State the blood parasite species.
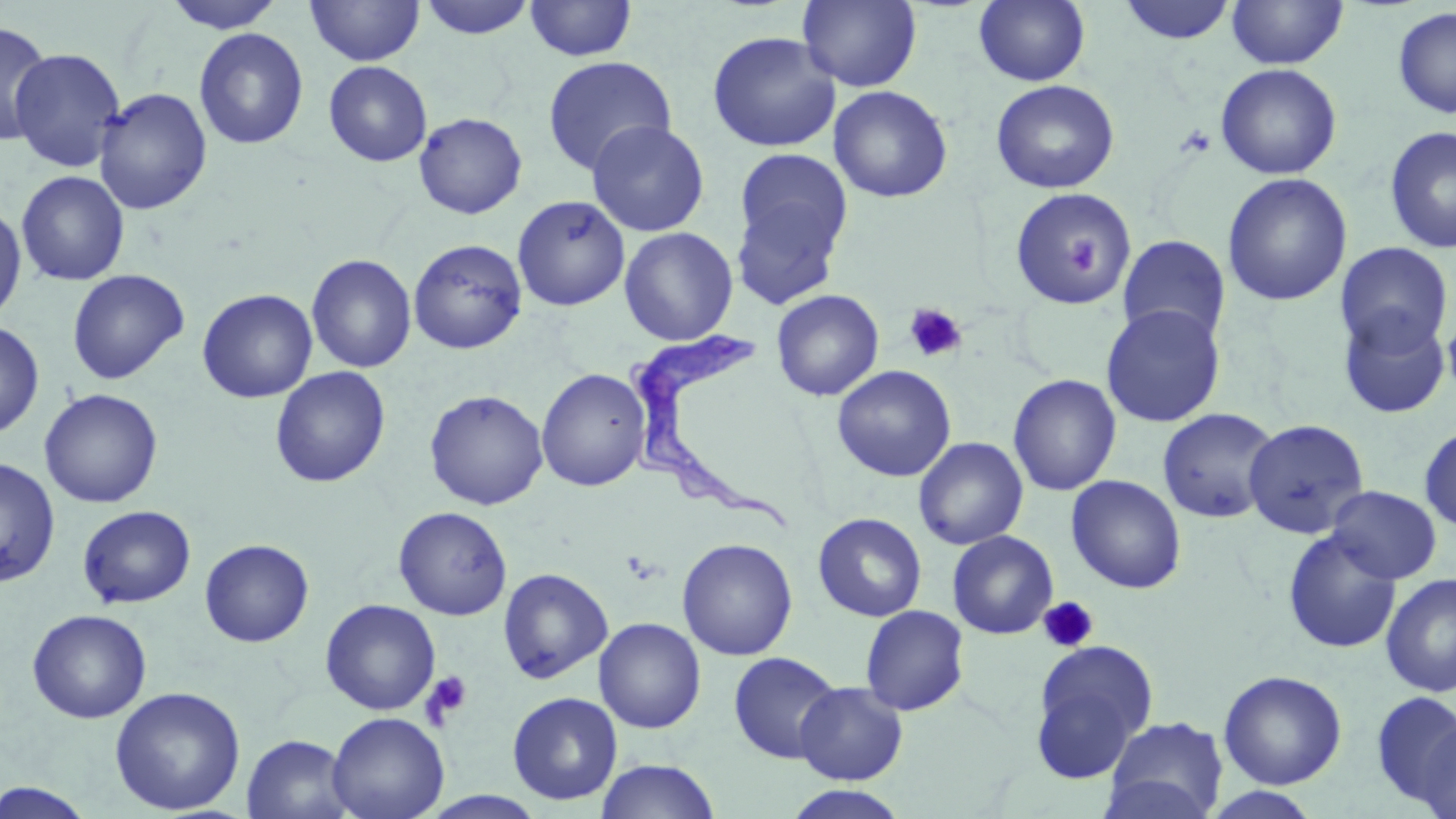
Trypanosoma brucei.

Approximate bounding boxes as (x1, y1, x2, y2) in pixels. Trypanosoma brucei locations: (625, 316, 796, 535). Uninfected red blood cell locations: (162, 0, 285, 34), (305, 0, 425, 66), (418, 0, 537, 41), (798, 0, 922, 91), (973, 0, 1090, 87), (1118, 0, 1237, 45), (1227, 0, 1348, 69), (524, 1, 637, 62), (1392, 6, 1456, 119), (1, 21, 54, 145), (194, 27, 308, 150), (707, 31, 841, 153), (9, 47, 126, 173), (542, 56, 676, 176), (323, 61, 432, 167), (1215, 63, 1341, 179), (990, 80, 1120, 193), (829, 85, 953, 203), (93, 87, 212, 215), (413, 112, 527, 219), (587, 120, 709, 237), (1384, 125, 1456, 253), (731, 163, 850, 306), (17, 171, 130, 285), (1222, 173, 1352, 307), (1008, 187, 1138, 307), (512, 194, 630, 311), (0, 204, 26, 325), (619, 227, 738, 345), (1117, 234, 1231, 346), (408, 239, 527, 354), (1335, 242, 1454, 358), (306, 253, 417, 373), (67, 269, 189, 385), (197, 288, 318, 403), (771, 289, 884, 401), (1101, 304, 1225, 427), (1337, 308, 1452, 419), (1441, 319, 1456, 400), (0, 320, 44, 439), (832, 364, 956, 482), (270, 366, 391, 488), (536, 368, 651, 492), (1007, 374, 1121, 496), (39, 388, 163, 508), (424, 389, 549, 510), (1157, 407, 1281, 524), (1242, 418, 1369, 539), (1419, 423, 1456, 533), (914, 437, 1028, 550), (0, 457, 60, 587), (1066, 475, 1186, 594), (1327, 485, 1442, 584), (78, 505, 196, 609), (393, 506, 512, 620), (812, 512, 926, 622), (1282, 529, 1401, 655), (947, 530, 1058, 639), (677, 538, 798, 661), (199, 539, 314, 648), (498, 567, 613, 684), (1380, 573, 1456, 697), (320, 599, 441, 715), (860, 605, 970, 716), (27, 609, 152, 723), (593, 617, 706, 733), (1028, 640, 1158, 783), (728, 651, 843, 764), (1219, 670, 1347, 790), (794, 681, 908, 785), (109, 686, 246, 815), (1372, 691, 1456, 808), (507, 692, 623, 805), (327, 712, 449, 819), (1101, 716, 1229, 819), (1418, 717, 1456, 819), (242, 734, 355, 819), (596, 758, 721, 819), (0, 780, 98, 818), (783, 785, 911, 819), (1202, 788, 1321, 818), (420, 791, 549, 818). Platelet locations: (1177, 125, 1216, 158), (903, 303, 967, 364), (1037, 596, 1098, 653), (420, 671, 473, 726). Thin blood smear. Single field of view. Light microscopy. Image is 1456×819 pixels. Captured at 1000x magnification. May-Grünwald-Giemsa stain.